Report the malaria status of this cell.
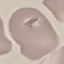

It is uninfected.

Cell patch, automatically extracted from a larger field of view and resized to 64 × 64 pixels. Photographed with a smartphone camera at the microscope eyepiece. Giemsa-stained preparation. Thin smear of blood.